Name the cell type shown.
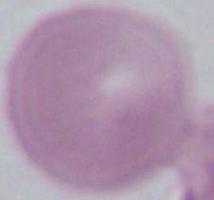
An erythrocyte.

Summary:
  - Modality: photomicrograph
  - Magnification: 1000x